Name the cell type shown.
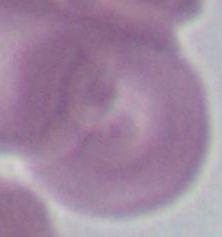

An erythrocyte.

modality: photomicrograph
magnification: 1000x